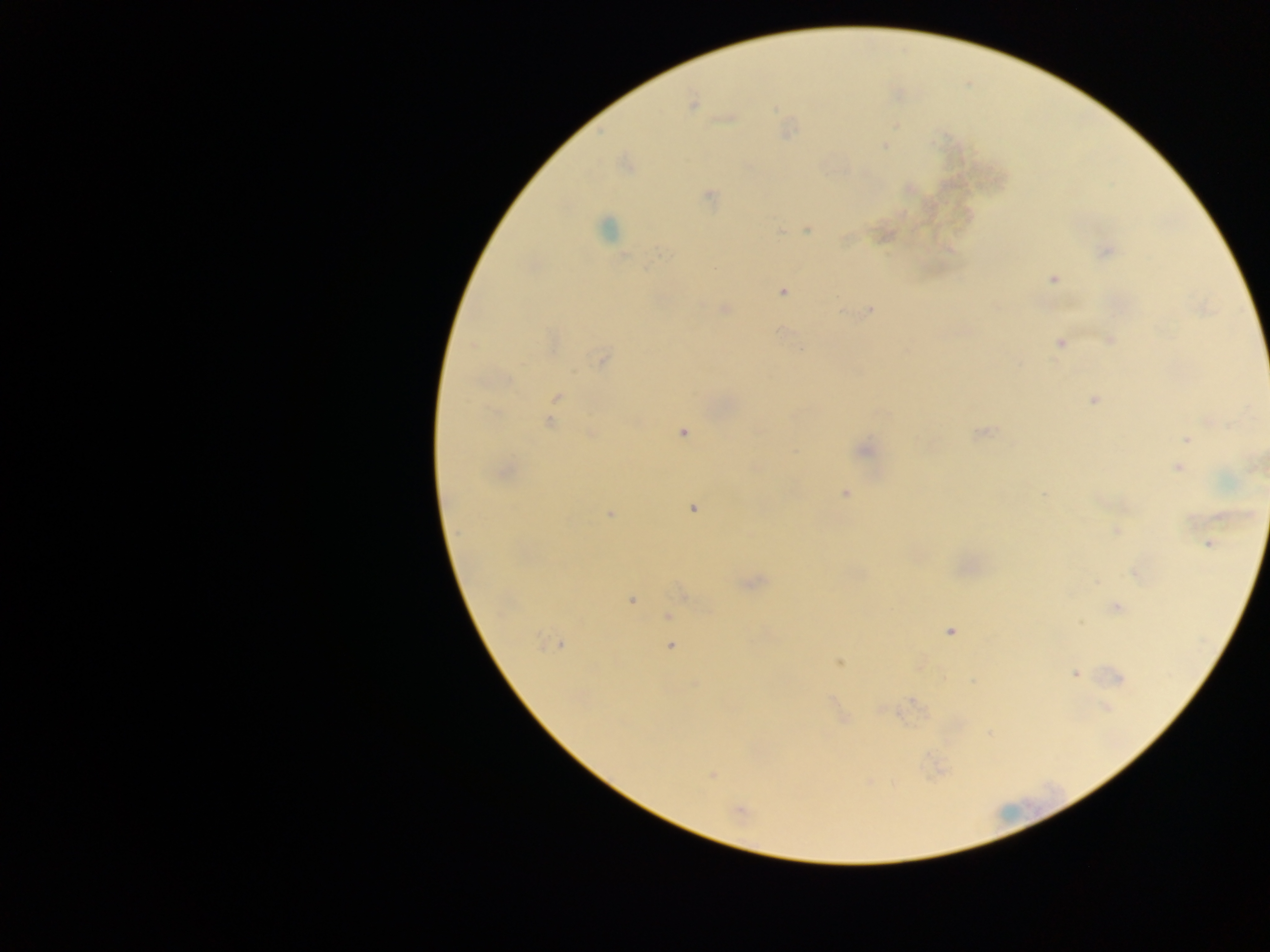
Approximate centers as {x, y} in pixels. Plasmodium parasite locations: {692, 103}, {726, 117}, {788, 130}, {884, 145}, {626, 164}, {908, 188}, {710, 197}, {607, 229}, {806, 229}, {781, 231}, {884, 233}, {1105, 251}, {1053, 279}, {782, 291}, {724, 309}, {868, 310}, {1109, 339}, {1060, 343}, {601, 358}, {556, 398}, {1093, 399}, {550, 420}, {682, 431}, {981, 433}, {591, 434}, {1186, 439}, {864, 448}, {1181, 458}, {1178, 468}, {503, 470}, {1042, 493}, {845, 494}, {692, 508}, {610, 513}, {1116, 530}, {1210, 543}, {1137, 571}, {750, 581}, {1098, 583}, {684, 594}, {630, 599}, {1115, 607}, {669, 615}, {1081, 622}, {948, 630}, {558, 643}, {669, 645}, {839, 661}, {1075, 673}, {1116, 677}, {1105, 707}, {883, 708}, {842, 717}, {989, 733}, {937, 769}, {711, 773}, {740, 810}. Collected in Ghana. Image is 1270×952 pixels. Thick blood smear. One field of view. Mobile-phone photograph taken through the microscope.